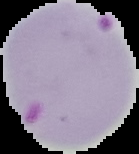 Image is 139×154 pixels. From a thin blood smear. Segmented cell region on a black background. Malaria status: parasitized.